Outline platelets.
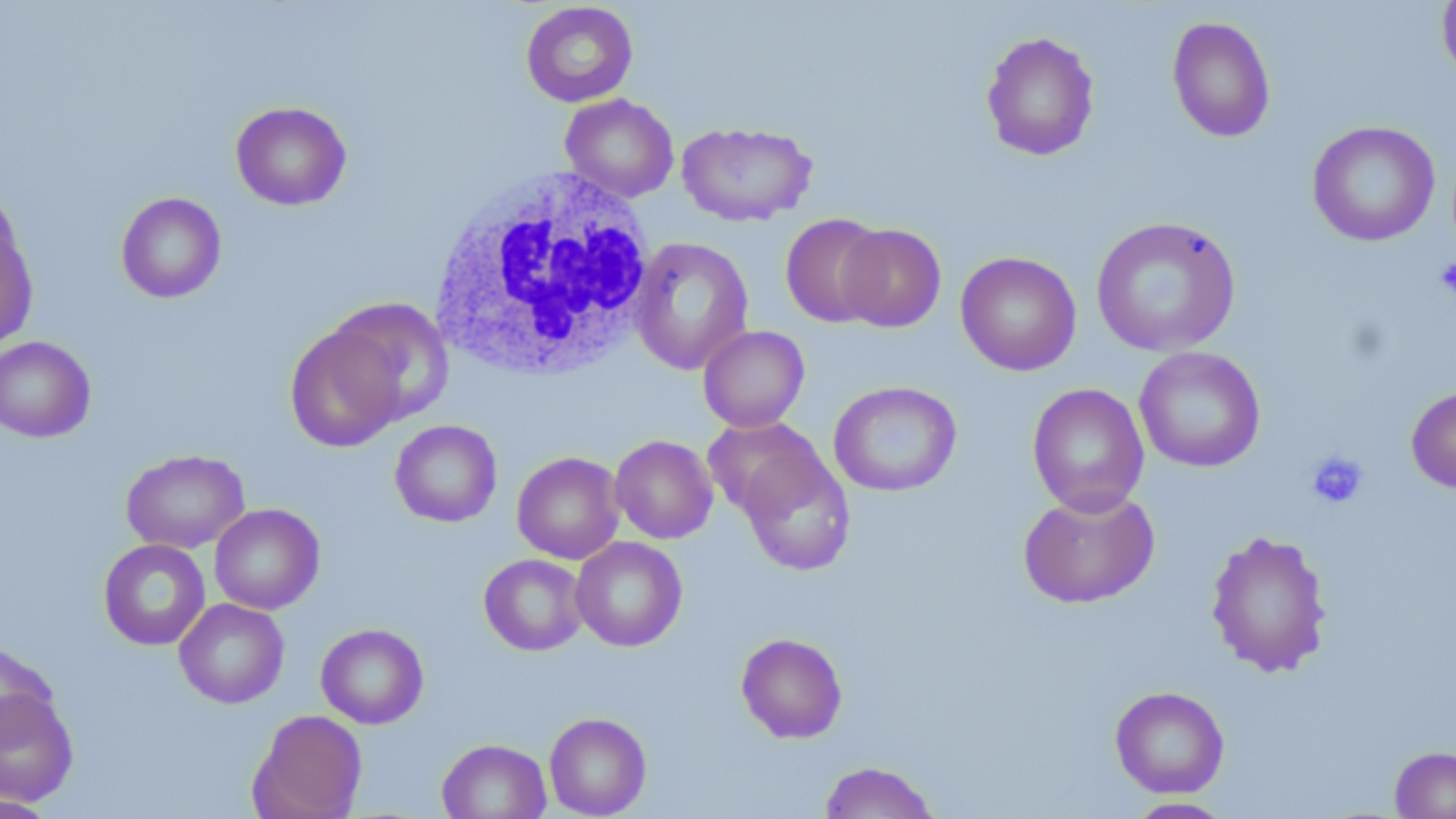

Approximate bounding boxes as (x1, y1, x2, y2) in pixels.
Platelets: (1434, 257, 1456, 300), (1305, 451, 1369, 510).

slide_level_diagnosis: negative for blood parasites
white_blood_cell_locations: 'approximate bounding boxes as (x1, y1, x2, y2) in pixels: (427, 163, 659, 384)'
modality: optical microscopy
uninfected_red_blood_cell_locations: 'approximate bounding boxes as (x1, y1, x2, y2) in pixels: (520, 2, 638, 107), (1436, 2, 1456, 83), (1167, 16, 1276, 144), (981, 31, 1100, 162), (560, 94, 679, 202), (230, 101, 352, 210), (676, 121, 817, 226), (1307, 121, 1440, 247), (0, 184, 25, 289), (115, 192, 227, 303), (780, 213, 888, 328), (0, 216, 38, 355), (1091, 216, 1240, 357), (835, 224, 946, 332), (629, 236, 755, 374), (955, 251, 1082, 376), (329, 298, 455, 427), (285, 323, 407, 453), (698, 325, 810, 432), (0, 336, 96, 443), (1134, 345, 1266, 473), (828, 380, 962, 497), (1027, 383, 1149, 516), (1406, 386, 1456, 493), (703, 417, 825, 520), (390, 420, 502, 527), (610, 435, 718, 544), (737, 446, 856, 576), (121, 449, 249, 554), (512, 451, 625, 564), (1018, 487, 1160, 609), (209, 503, 325, 614), (1205, 529, 1333, 679), (570, 537, 688, 652), (98, 539, 211, 650), (479, 553, 589, 656), (174, 598, 289, 708), (316, 623, 429, 729), (735, 632, 848, 744), (0, 641, 58, 742), (1110, 685, 1230, 798), (0, 687, 79, 806), (247, 709, 367, 819), (544, 712, 652, 818), (437, 738, 552, 818), (1389, 745, 1456, 819), (819, 761, 941, 819), (0, 795, 60, 818), (1123, 797, 1237, 818)'
stain: May-Grünwald-Giemsa
magnification: 1000x
preparation: thin blood smear
image_size: 1456×819 pixels
field_of_view: one of a larger specimen